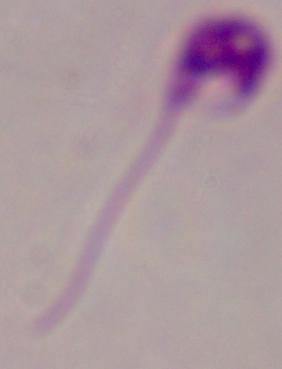 Captured at 1000x magnification. Micrograph. A Leishmania parasite is shown.